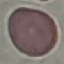

malaria_status: uninfected
preparation: thin smear
capture: smartphone through the microscope eyepiece
image_type: cell patch, automatically extracted from a larger field of view and resized to 64 × 64 pixels
stain: Giemsa